Name the parasite shown.
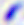
This is Toxoplasma gondii.

400x magnification. Micrograph.